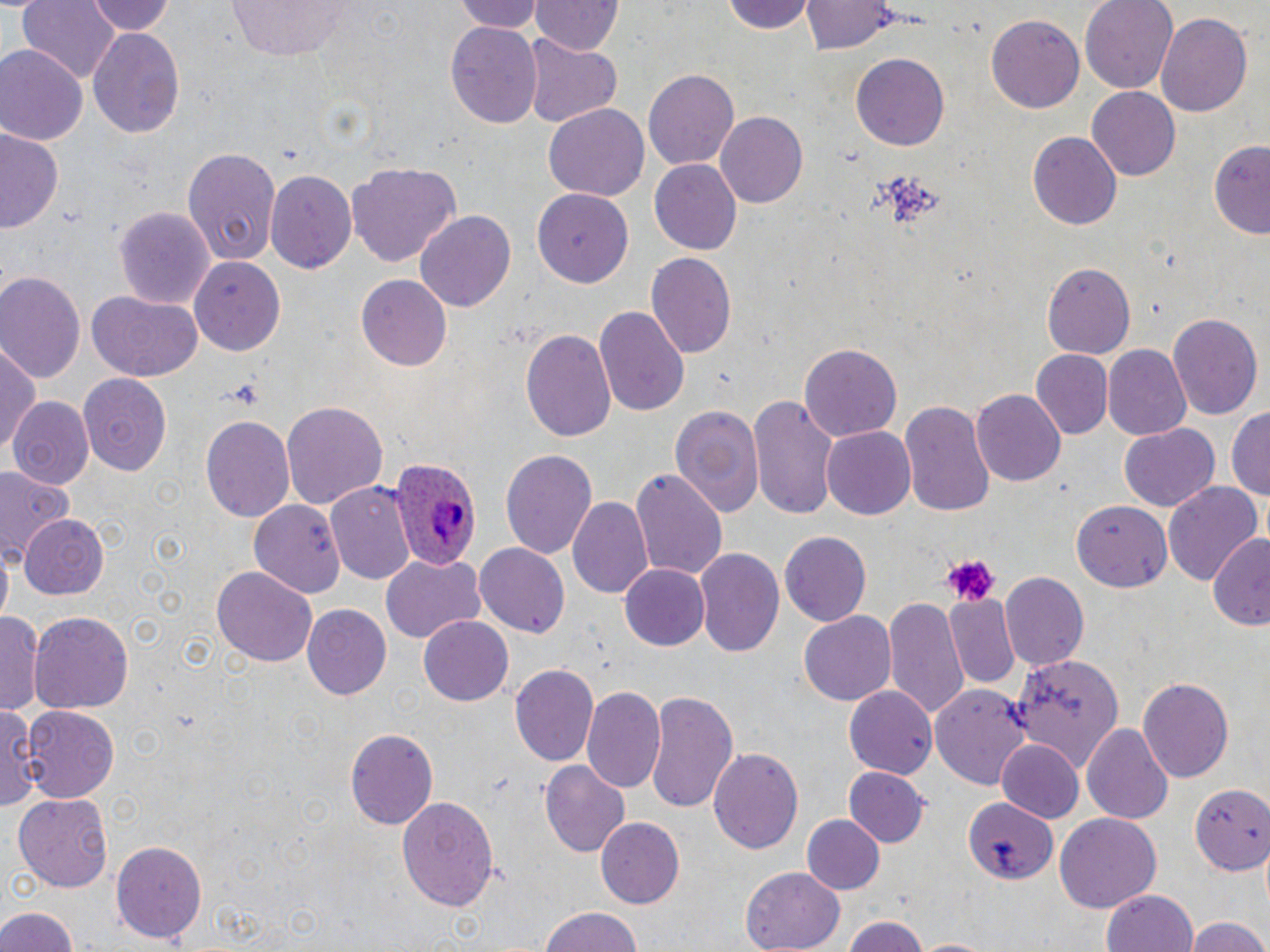
Approximate bounding boxes as (x1,y1)-(x2,y2) corner pairs in pixels. Platelet locations: (937,554)-(1000,605). Plasmodium ovale-infected red blood cell locations: (383,455)-(479,571). Uninfected red blood cell locations: (18,0)-(120,87), (86,0)-(176,36), (225,0)-(361,58), (455,0)-(541,33), (719,0)-(821,35), (803,0)-(893,54), (1083,0)-(1179,93), (530,1)-(622,57), (1155,11)-(1254,117), (986,15)-(1086,113), (444,19)-(542,129), (86,24)-(184,139), (522,37)-(623,128), (0,45)-(85,146), (851,51)-(950,150), (643,68)-(739,171), (1088,87)-(1181,181), (544,104)-(649,202), (712,109)-(808,207), (0,128)-(63,235), (1027,130)-(1122,229), (1210,137)-(1270,237), (182,146)-(279,266), (650,160)-(741,253), (347,162)-(460,269), (264,166)-(356,271), (531,190)-(634,288), (115,204)-(216,308), (417,209)-(516,313), (646,252)-(736,359), (189,257)-(285,356), (1042,261)-(1136,357), (0,270)-(86,387), (356,275)-(452,373), (85,290)-(204,380), (595,303)-(690,420), (1167,311)-(1261,418), (520,327)-(618,442), (1,341)-(40,457), (800,344)-(902,442), (1105,346)-(1192,440), (1029,350)-(1114,440), (76,372)-(173,475), (973,390)-(1065,487), (748,395)-(839,518), (12,398)-(93,490), (900,398)-(996,521), (281,400)-(387,510), (672,403)-(765,517), (1228,408)-(1269,506), (200,415)-(294,527), (1119,424)-(1218,514), (820,426)-(914,520), (500,449)-(597,562), (0,465)-(73,563), (631,468)-(726,581), (327,482)-(418,590), (1164,482)-(1264,588), (568,496)-(654,601), (249,499)-(344,596), (1073,500)-(1172,590), (21,516)-(108,598), (781,530)-(874,626), (1207,532)-(1270,628), (473,545)-(569,636), (694,548)-(784,658), (381,553)-(485,644), (620,563)-(709,651), (212,566)-(315,668), (1000,571)-(1088,668), (884,593)-(971,723), (945,595)-(1021,690), (302,604)-(392,698), (1,609)-(43,719), (28,609)-(134,715), (799,611)-(896,707), (420,615)-(513,706), (1012,653)-(1126,768), (508,662)-(599,766), (1138,678)-(1234,781), (843,684)-(939,780), (930,684)-(1035,793), (583,685)-(667,795), (645,690)-(738,815), (22,703)-(120,801), (0,704)-(39,813), (1082,723)-(1172,825), (344,727)-(437,829), (995,739)-(1085,823), (708,747)-(804,856), (539,763)-(629,854), (845,767)-(930,846), (1189,783)-(1270,872), (12,793)-(115,892), (396,793)-(499,909), (960,796)-(1057,881), (1055,812)-(1162,911), (802,815)-(884,894), (597,817)-(684,907), (112,838)-(210,942), (741,867)-(845,951), (1102,889)-(1199,952), (0,904)-(84,952), (538,909)-(645,952), (840,915)-(925,952), (1185,915)-(1270,952), (912,937)-(993,952). Slide-level diagnosis: Plasmodium ovale. Captured at 1000x magnification. Image is 1270×952 pixels. Optical microscopy. Single field of view. May-Grünwald-Giemsa stain. Thin blood smear.